Point out Plasmodium parasites and leukocytes.
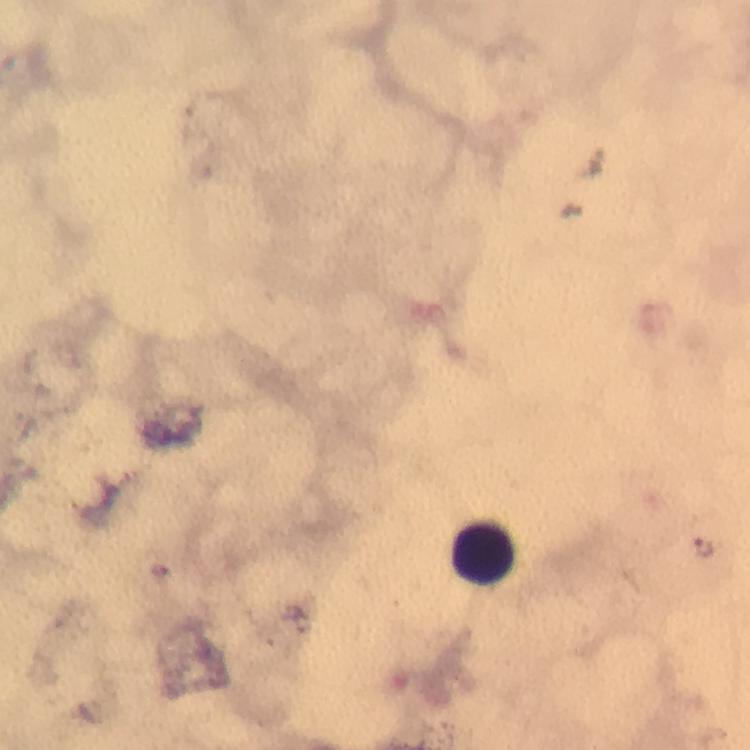
Approximate centers as [x, y] in pixels.
Plasmodium parasites: [702, 547].
Leukocytes: [484, 552].

Summary:
  - Preparation: thick blood smear
  - Context: from a diagnostic examination for malaria
  - Capture: smartphone mounted on the microscope
  - Immersion oil: applied
  - Cropped from: a single field of view
  - Stain: Giemsa
  - Magnification: 100x
  - Image size: 750×750 pixels